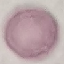

Summary:
  - Malaria status: uninfected
  - Preparation: thin blood film
  - Capture: smartphone camera at the microscope eyepiece
  - Image type: cell patch, automatically extracted from a larger field of view and resized to 64 × 64 pixels
  - Stain: Giemsa